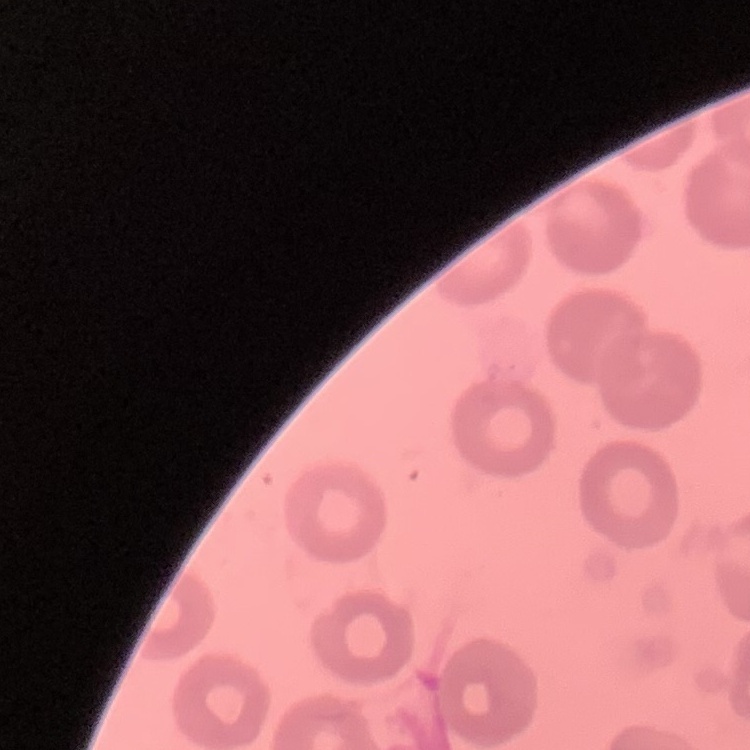 The red blood cells show no rouleaux formation. Stained with either Field's or Giemsa. Square crop of a larger photomicrograph. Thin blood smear.